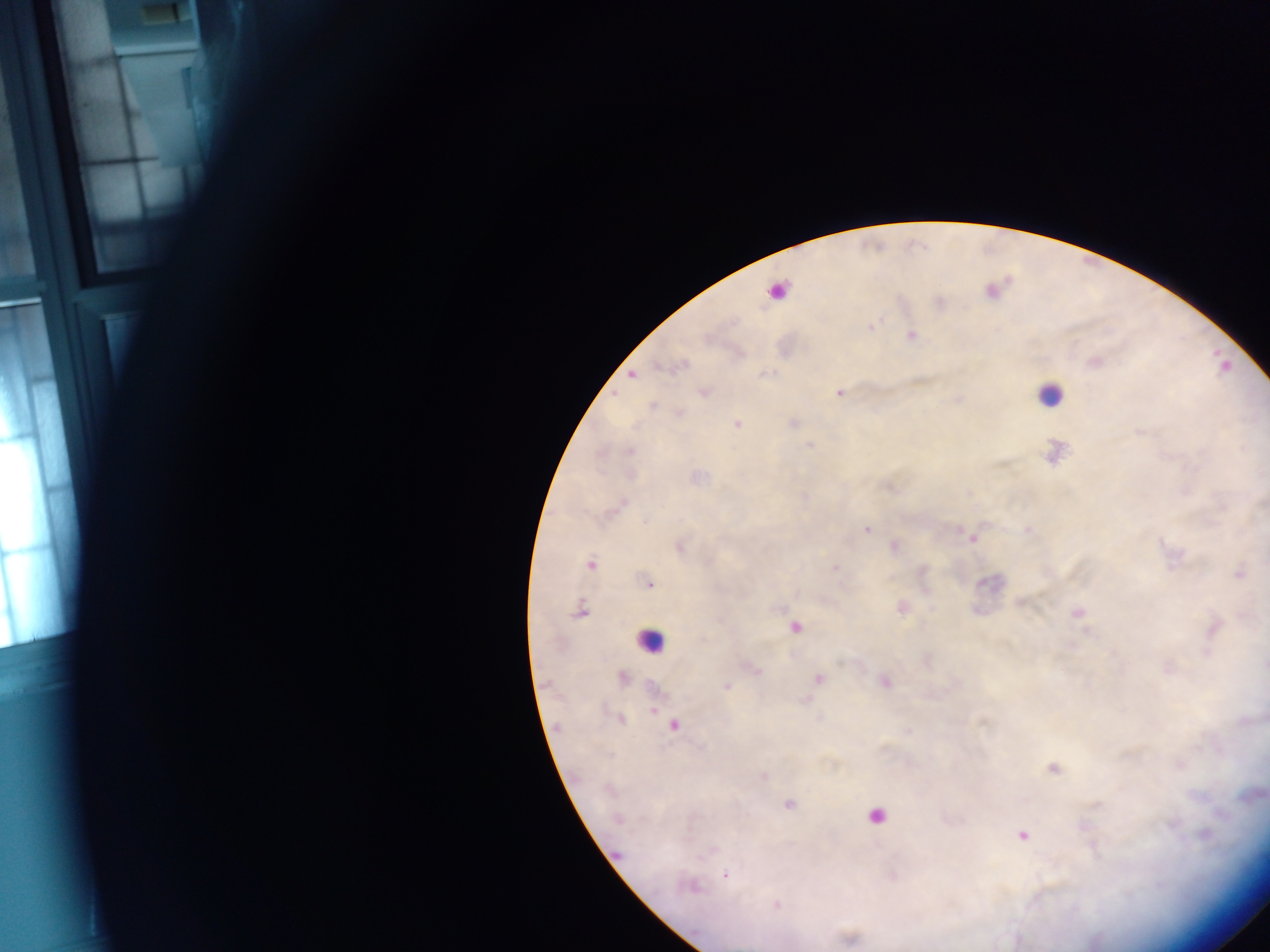
Approximate centers as (x, y) in pixels.
Summary:
  - Plasmodium parasite locations: (159, 19), (1093, 362), (632, 375), (838, 391), (1139, 431), (809, 444), (866, 529), (973, 539), (592, 565), (835, 567), (650, 581), (725, 688), (653, 711), (672, 725), (788, 806), (875, 816), (1022, 835), (725, 875)
  - Leukocyte locations: (646, 644)
  - Capture: mobile-phone photograph through a microscope
  - Field of view: single
  - Image size: 1270×952 pixels
  - Country: Ghana
  - Preparation: thick blood film